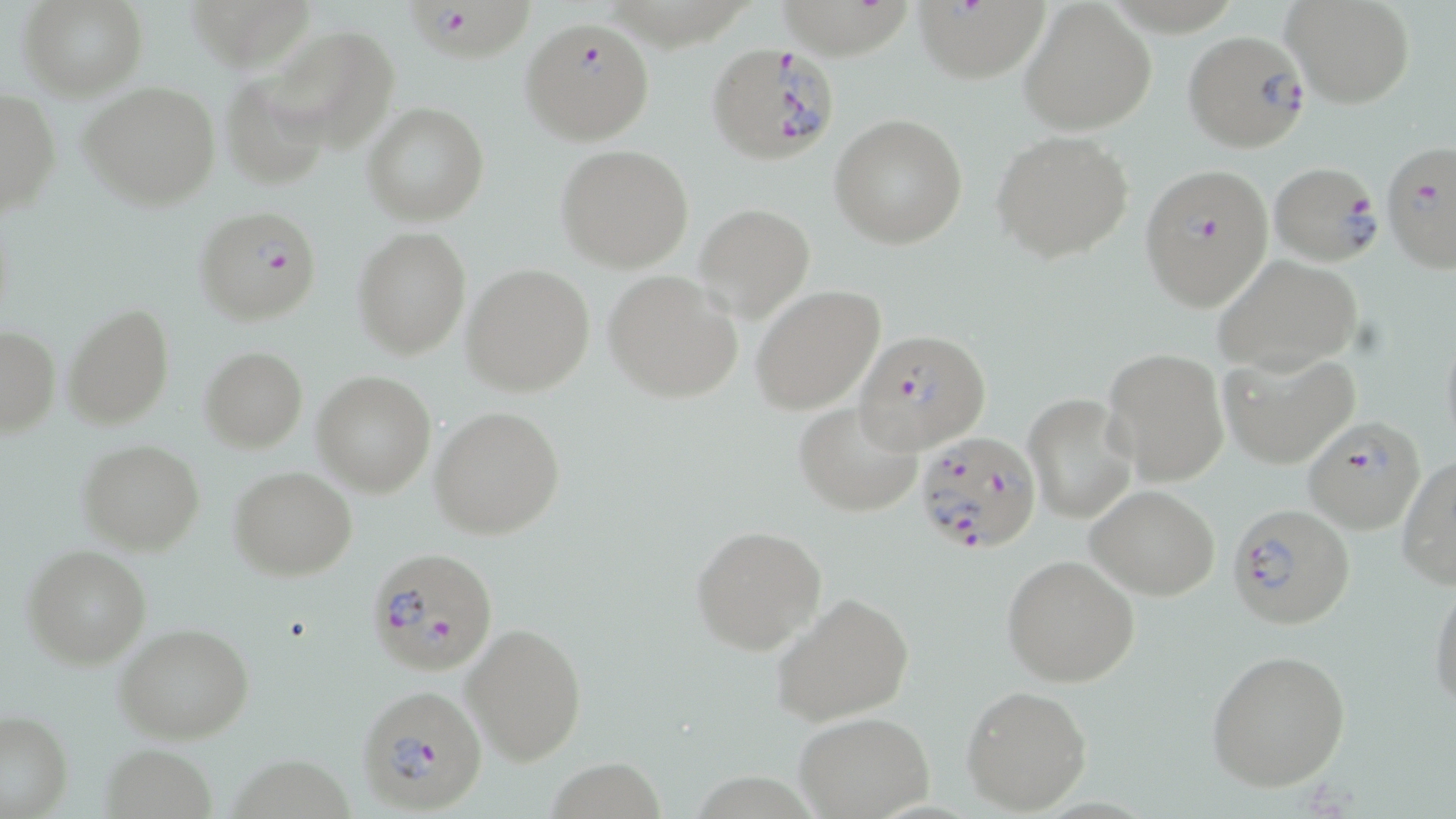

slide-level diagnosis = Plasmodium falciparum
modality = light microscopy
image size = 1456×819 pixels
stain = May-Grünwald-Giemsa
field of view = one of a larger specimen
Plasmodium falciparum-infected red blood cell locations (subset) = approximate bounding boxes as (x1,y1)-(x2,y2) corner pairs in pixels: (399,0)-(532,63), (916,0)-(1064,91), (521,19)-(655,144), (1181,31)-(1312,154), (1380,137)-(1456,276), (1269,162)-(1385,267), (1138,163)-(1276,313), (194,204)-(321,326), (858,327)-(993,453), (1303,414)-(1426,535), (913,431)-(1043,558), (1230,503)-(1357,629), (363,547)-(498,675), (358,684)-(488,814)
uninfected red blood cell locations (subset) = approximate bounding boxes as (x1,y1)-(x2,y2) corner pairs in pixels: (21,0)-(146,100), (1283,0)-(1415,109), (185,1)-(320,74), (1018,1)-(1155,134), (253,25)-(400,156), (79,80)-(223,211), (0,90)-(60,216), (362,103)-(488,225), (830,113)-(968,248), (991,129)-(1135,264), (555,145)-(694,272), (693,203)-(815,322), (352,226)-(470,359), (1212,255)-(1364,374), (463,263)-(595,397), (602,270)-(743,403), (753,284)-(885,415), (62,303)-(174,430), (1,327)-(60,437), (200,346)-(306,453), (1102,348)-(1230,486), (1220,350)-(1360,469), (312,371)-(436,495), (1021,392)-(1138,524), (794,400)-(924,517), (430,406)-(564,539), (77,440)-(204,555), (1396,453)-(1456,590), (230,467)-(357,580), (1087,485)-(1221,599), (689,524)-(826,655), (23,545)-(150,669), (1001,554)-(1141,688), (1428,572)-(1456,717), (772,591)-(915,726), (462,619)-(588,766), (113,623)-(254,744), (1204,649)-(1353,791), (961,685)-(1094,815), (0,710)-(73,817), (793,712)-(934,817), (100,743)-(218,818), (231,759)-(358,819)
magnification = 1000x
preparation = thin blood film